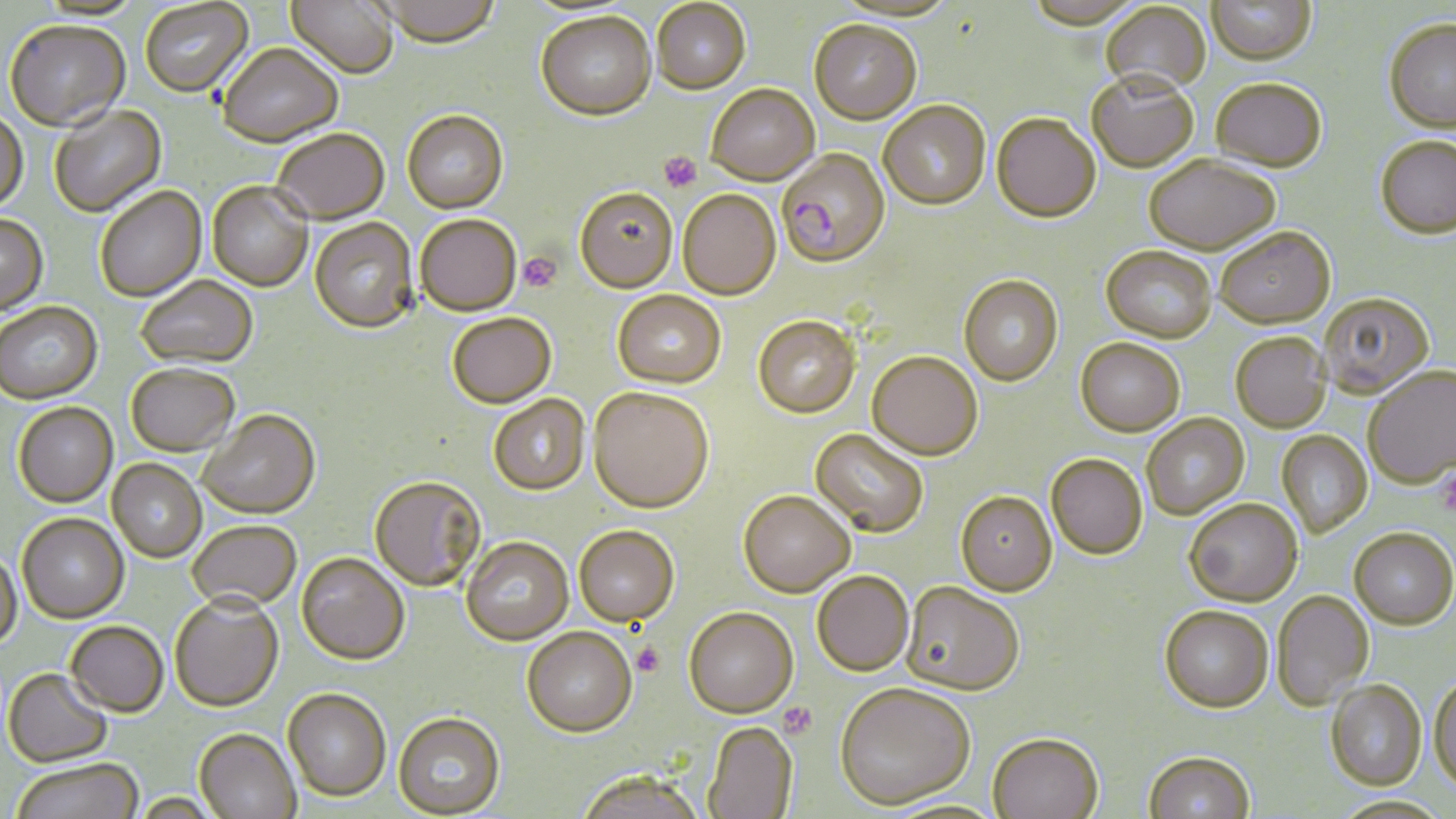 Approximate bounding boxes as named x1/y1/x2/y2 corners in pixels. Uninfected red blood cell locations: (x1=140, y1=0, x2=253, y2=99), (x1=286, y1=0, x2=399, y2=80), (x1=378, y1=0, x2=501, y2=49), (x1=651, y1=0, x2=751, y2=95), (x1=31, y1=1, x2=144, y2=23), (x1=1206, y1=1, x2=1316, y2=65), (x1=1101, y1=2, x2=1211, y2=94), (x1=535, y1=13, x2=657, y2=123), (x1=1383, y1=18, x2=1456, y2=133), (x1=809, y1=21, x2=921, y2=124), (x1=4, y1=22, x2=131, y2=133), (x1=217, y1=46, x2=343, y2=148), (x1=1087, y1=73, x2=1198, y2=172), (x1=1211, y1=77, x2=1327, y2=172), (x1=706, y1=84, x2=819, y2=186), (x1=878, y1=100, x2=991, y2=210), (x1=49, y1=106, x2=167, y2=218), (x1=402, y1=110, x2=508, y2=214), (x1=0, y1=111, x2=29, y2=215), (x1=992, y1=113, x2=1101, y2=222), (x1=272, y1=129, x2=389, y2=225), (x1=1375, y1=135, x2=1456, y2=238), (x1=1144, y1=155, x2=1280, y2=255), (x1=207, y1=182, x2=313, y2=292), (x1=95, y1=187, x2=207, y2=302), (x1=574, y1=187, x2=678, y2=293), (x1=677, y1=190, x2=781, y2=300), (x1=0, y1=214, x2=48, y2=317), (x1=415, y1=214, x2=522, y2=316), (x1=309, y1=218, x2=419, y2=333), (x1=1215, y1=226, x2=1335, y2=328), (x1=1101, y1=245, x2=1216, y2=342), (x1=958, y1=274, x2=1063, y2=385), (x1=136, y1=276, x2=258, y2=369), (x1=612, y1=289, x2=726, y2=388), (x1=1318, y1=293, x2=1435, y2=399), (x1=0, y1=302, x2=103, y2=406), (x1=447, y1=312, x2=556, y2=408), (x1=753, y1=315, x2=861, y2=418), (x1=1230, y1=332, x2=1331, y2=432), (x1=1076, y1=338, x2=1185, y2=435), (x1=867, y1=351, x2=983, y2=460), (x1=126, y1=365, x2=240, y2=458), (x1=1363, y1=366, x2=1456, y2=489), (x1=588, y1=387, x2=714, y2=513), (x1=489, y1=395, x2=590, y2=495), (x1=13, y1=404, x2=118, y2=509), (x1=198, y1=410, x2=320, y2=520), (x1=1141, y1=413, x2=1250, y2=520), (x1=810, y1=428, x2=929, y2=537), (x1=1276, y1=430, x2=1373, y2=538), (x1=1046, y1=453, x2=1147, y2=559), (x1=107, y1=459, x2=206, y2=563), (x1=370, y1=475, x2=486, y2=591), (x1=738, y1=490, x2=854, y2=596), (x1=955, y1=490, x2=1057, y2=596), (x1=1184, y1=499, x2=1302, y2=606), (x1=17, y1=515, x2=129, y2=625), (x1=188, y1=521, x2=301, y2=612), (x1=573, y1=524, x2=679, y2=626), (x1=1350, y1=529, x2=1456, y2=630), (x1=461, y1=536, x2=573, y2=645), (x1=0, y1=551, x2=23, y2=652), (x1=297, y1=552, x2=410, y2=665), (x1=811, y1=570, x2=914, y2=675), (x1=900, y1=582, x2=1025, y2=696), (x1=1272, y1=590, x2=1374, y2=709), (x1=170, y1=596, x2=284, y2=713), (x1=1159, y1=605, x2=1274, y2=712), (x1=683, y1=607, x2=798, y2=717), (x1=65, y1=623, x2=168, y2=719), (x1=522, y1=627, x2=637, y2=736), (x1=3, y1=670, x2=113, y2=769), (x1=1429, y1=674, x2=1456, y2=793), (x1=1325, y1=681, x2=1427, y2=790), (x1=834, y1=682, x2=975, y2=809), (x1=282, y1=688, x2=391, y2=801), (x1=393, y1=712, x2=505, y2=817), (x1=703, y1=720, x2=798, y2=818), (x1=193, y1=729, x2=301, y2=819), (x1=987, y1=731, x2=1104, y2=819), (x1=1143, y1=752, x2=1256, y2=818), (x1=11, y1=762, x2=143, y2=819), (x1=575, y1=770, x2=706, y2=819). Plasmodium falciparum-infected red blood cell locations: (x1=776, y1=148, x2=891, y2=267). Platelet locations: (x1=658, y1=151, x2=702, y2=193), (x1=517, y1=251, x2=562, y2=293), (x1=1437, y1=467, x2=1456, y2=519), (x1=632, y1=642, x2=665, y2=676), (x1=779, y1=702, x2=818, y2=738). Slide-level diagnosis: Plasmodium falciparum. May-Grünwald-Giemsa stain. One field of a larger specimen. 1000x magnification. Thin blood smear. Image is 1456×819 pixels. Optical microscopy.